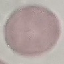
Summary:
  - Result: negative for malaria parasites
  - Capture: smartphone through the microscope eyepiece
  - Stain: Giemsa
  - Image type: cell patch, automatically extracted from a larger field of view and resized to 64 × 64 pixels
  - Preparation: thin blood film